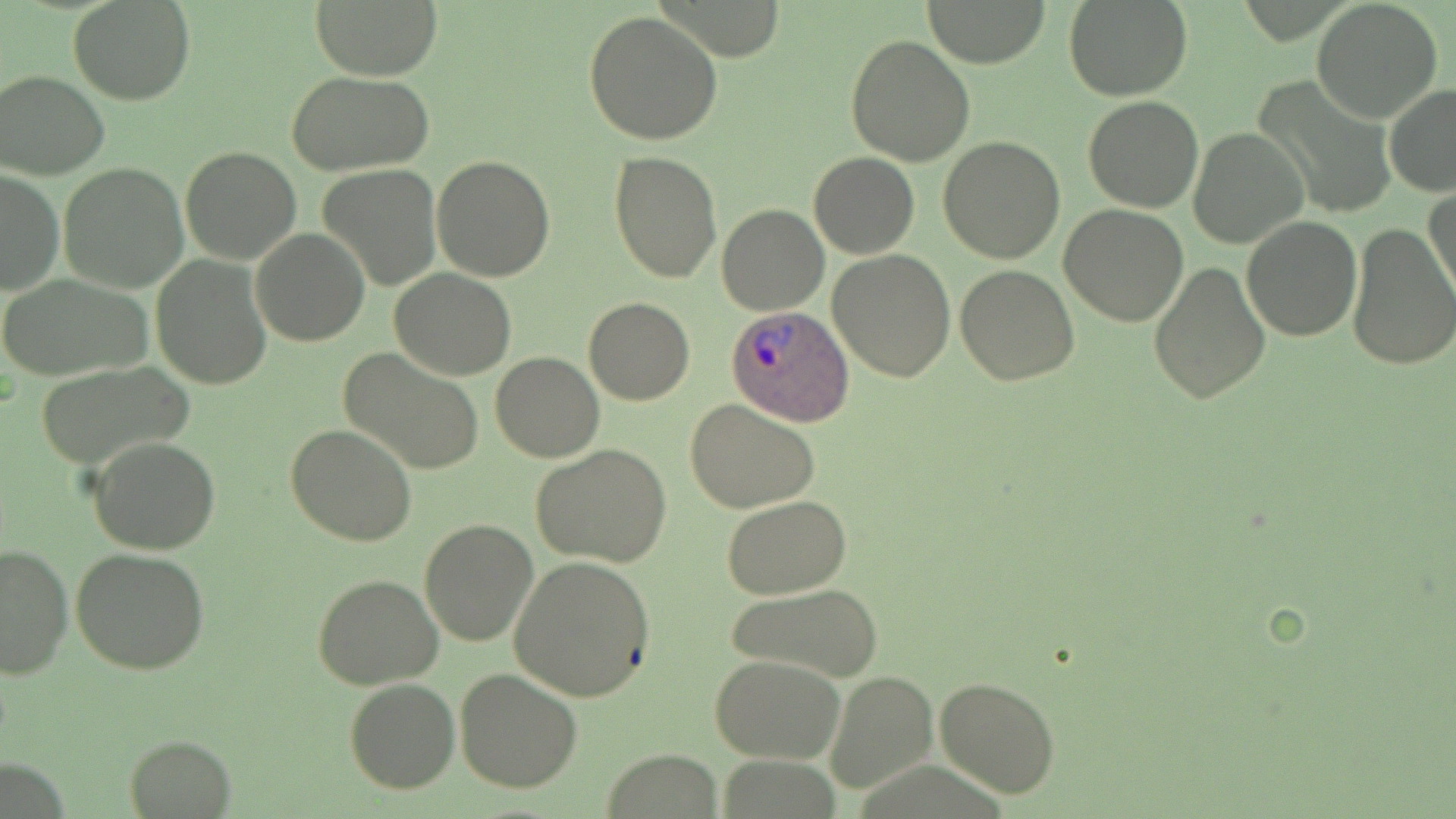 Approximate bounding boxes as named x1/y1/x2/y2 corners in pixels. Uninfected red blood cell locations: (x1=68, y1=0, x2=195, y2=104), (x1=310, y1=0, x2=442, y2=80), (x1=1063, y1=0, x2=1194, y2=101), (x1=924, y1=1, x2=1053, y2=67), (x1=1310, y1=2, x2=1442, y2=121), (x1=583, y1=10, x2=724, y2=147), (x1=844, y1=35, x2=975, y2=167), (x1=0, y1=69, x2=113, y2=180), (x1=285, y1=69, x2=434, y2=177), (x1=1255, y1=81, x2=1391, y2=220), (x1=1383, y1=83, x2=1456, y2=197), (x1=1082, y1=96, x2=1203, y2=212), (x1=1187, y1=127, x2=1308, y2=249), (x1=938, y1=136, x2=1068, y2=263), (x1=178, y1=145, x2=303, y2=266), (x1=609, y1=151, x2=722, y2=283), (x1=808, y1=152, x2=918, y2=258), (x1=431, y1=155, x2=557, y2=282), (x1=57, y1=163, x2=190, y2=293), (x1=318, y1=164, x2=443, y2=291), (x1=0, y1=168, x2=63, y2=298), (x1=1425, y1=185, x2=1456, y2=304), (x1=716, y1=203, x2=829, y2=316), (x1=1058, y1=203, x2=1188, y2=327), (x1=1241, y1=214, x2=1363, y2=340), (x1=1345, y1=222, x2=1456, y2=372), (x1=250, y1=228, x2=371, y2=346), (x1=827, y1=250, x2=955, y2=382), (x1=150, y1=253, x2=273, y2=390), (x1=1149, y1=260, x2=1271, y2=404), (x1=954, y1=265, x2=1080, y2=385), (x1=391, y1=268, x2=515, y2=379), (x1=0, y1=272, x2=153, y2=381), (x1=584, y1=297, x2=695, y2=405), (x1=338, y1=347, x2=485, y2=476), (x1=490, y1=351, x2=605, y2=461), (x1=36, y1=362, x2=192, y2=472), (x1=686, y1=398, x2=819, y2=512), (x1=284, y1=423, x2=416, y2=549), (x1=87, y1=435, x2=222, y2=554), (x1=532, y1=443, x2=673, y2=569), (x1=723, y1=496, x2=851, y2=600), (x1=419, y1=519, x2=539, y2=646), (x1=0, y1=542, x2=73, y2=680), (x1=69, y1=548, x2=211, y2=678), (x1=507, y1=557, x2=657, y2=701), (x1=313, y1=574, x2=444, y2=691), (x1=726, y1=582, x2=886, y2=682), (x1=711, y1=654, x2=844, y2=764), (x1=454, y1=668, x2=582, y2=792), (x1=825, y1=670, x2=938, y2=793), (x1=934, y1=676, x2=1060, y2=800), (x1=343, y1=678, x2=460, y2=794), (x1=125, y1=734, x2=236, y2=815), (x1=603, y1=749, x2=723, y2=817). Plasmodium ovale-infected red blood cell locations: (x1=725, y1=303, x2=852, y2=426). Slide-level diagnosis: Plasmodium ovale. Thin blood smear. May-Grünwald-Giemsa-stained preparation. Image is 1456×819 pixels. Single field of view. Light microscopy. 1000x magnification.